Name the cell type shown.
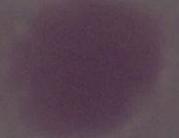
This is an erythrocyte.

Summary:
  - Modality: photomicrograph
  - Magnification: 1000x